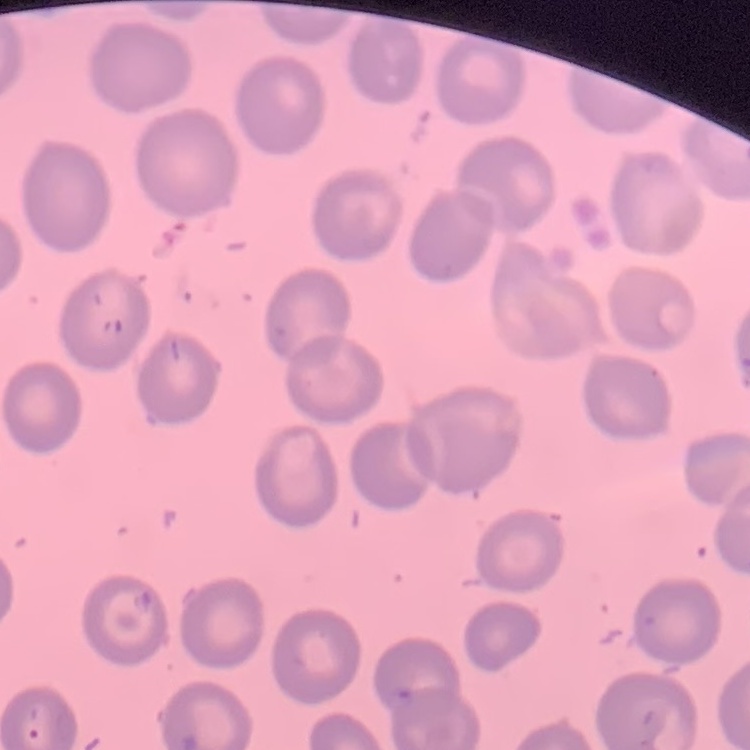

erythrocyte morphology = no rouleaux formation
image type = one tile cut from a larger photomicrograph
preparation = thin peripheral smear
stain = Field's or Giemsa